Identify the blood parasite species.
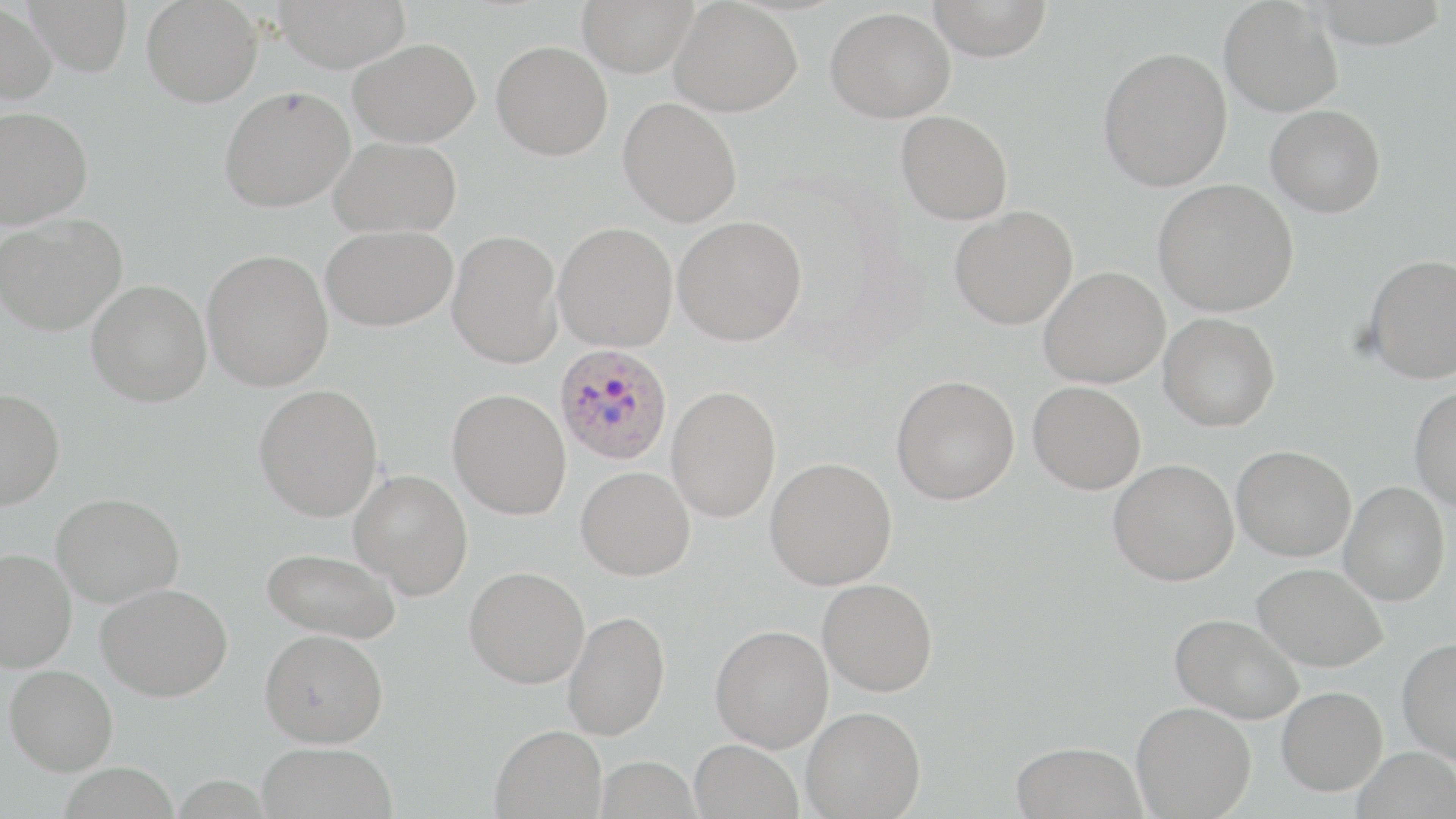

Plasmodium ovale.

{
  "magnification": "1000x",
  "plasmodium_ovale_infected_red_blood_cell_locations": "approximate bounding boxes as [x1, y1, x2, y2] in pixels: [554, 343, 673, 465]",
  "stain": "May-Grünwald-Giemsa",
  "uninfected_red_blood_cell_locations": "approximate bounding boxes as [x1, y1, x2, y2] in pixels: [24, 0, 133, 76], [142, 0, 263, 107], [273, 0, 411, 71], [577, 0, 698, 77], [927, 0, 1054, 60], [670, 1, 802, 116], [1219, 1, 1343, 117], [0, 2, 58, 105], [825, 7, 955, 122], [349, 38, 480, 147], [492, 40, 613, 160], [1098, 46, 1233, 192], [219, 86, 354, 212], [618, 97, 742, 226], [1265, 105, 1385, 217], [0, 106, 93, 228], [896, 110, 1013, 225], [329, 135, 462, 238], [1153, 178, 1298, 317], [950, 206, 1078, 330], [0, 213, 127, 335], [673, 215, 807, 346], [553, 222, 678, 351], [321, 224, 458, 331], [447, 230, 563, 368], [201, 249, 333, 392], [1363, 254, 1456, 384], [1040, 267, 1170, 388], [86, 280, 212, 407], [1158, 313, 1280, 432], [891, 375, 1020, 504], [1028, 381, 1145, 494], [254, 384, 383, 521], [666, 385, 781, 523], [1409, 385, 1456, 510], [0, 388, 65, 510], [447, 388, 571, 520], [1231, 445, 1356, 561], [765, 457, 897, 590], [1108, 458, 1239, 586], [576, 466, 695, 580], [349, 469, 472, 600], [1339, 482, 1450, 606], [51, 492, 184, 607], [0, 547, 77, 672], [262, 547, 402, 644], [1252, 562, 1388, 671], [464, 566, 589, 689], [818, 578, 938, 696], [96, 582, 233, 701], [562, 610, 670, 740], [1170, 613, 1304, 724], [710, 624, 833, 752], [259, 628, 388, 748], [1397, 637, 1456, 765], [4, 664, 119, 775], [1277, 686, 1387, 795], [1131, 701, 1256, 819], [801, 706, 926, 818], [490, 724, 606, 819], [689, 739, 803, 819], [1010, 741, 1147, 819], [256, 742, 398, 819], [1353, 746, 1456, 819], [595, 755, 701, 818]",
  "preparation": "thin blood film",
  "modality": "optical microscopy",
  "field_of_view": "single",
  "image_size": "1456×819 pixels"
}